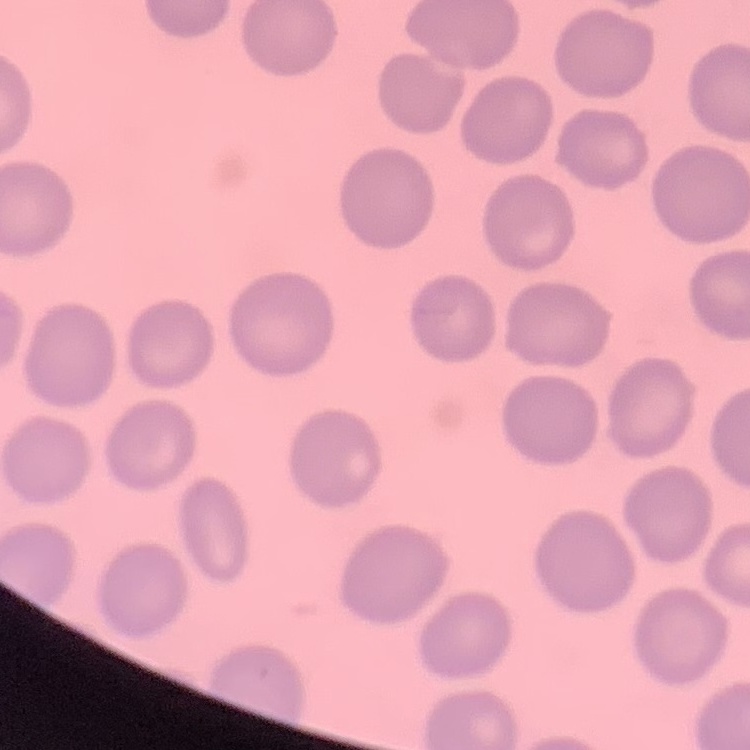

The erythrocytes show no rouleaux formation. Thin peripheral smear. One tile cut from a larger photomicrograph. Stained with either Field's or Giemsa.